Classify this cell by malaria status.
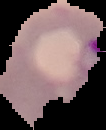

Parasitized.

Summary:
  - Image type: segmented cell region on a black background
  - Image size: 106×130 pixels
  - Preparation: thin blood smear